Name the parasite shown.
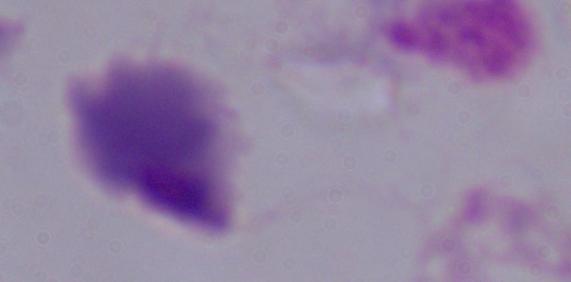
A trichomonad.

Summary:
  - Modality: photomicrograph
  - Magnification: 1000x